Report the malaria status of this cell.
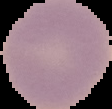

Uninfected.

Image is 112×109 pixels. The area outside the segmented cell region is set to black. From a thin blood smear.